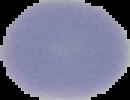

malaria status = uninfected
image type = segmented cell region with the area outside set to black
preparation = thin blood film
image size = 130×100 pixels